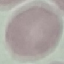

Result: no malaria parasites seen. Photographed with a smartphone camera at the microscope eyepiece. Thin smear of blood. Giemsa-stained preparation. Automatically extracted cell patch, resized to 64 × 64 pixels.